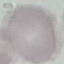 Result: no malaria parasites detected. Cell patch, automatically extracted from a larger field of view and resized to 64 × 64 pixels. Giemsa-stained preparation. Acquired by smartphone through the microscope eyepiece. Thin smear of blood.